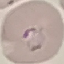

malaria status = parasitized
image type = automatically extracted cell patch, resized to 64 × 64 pixels
preparation = thin smear
stain = Giemsa
capture = smartphone through the microscope eyepiece